Assess this cell for malaria.
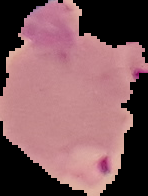
Parasitized.

Summary:
  - Image type: cell region segmented out of the field of view; surrounding area masked to black
  - Image size: 148×196 pixels
  - Preparation: thin blood film